Evaluate for malaria.
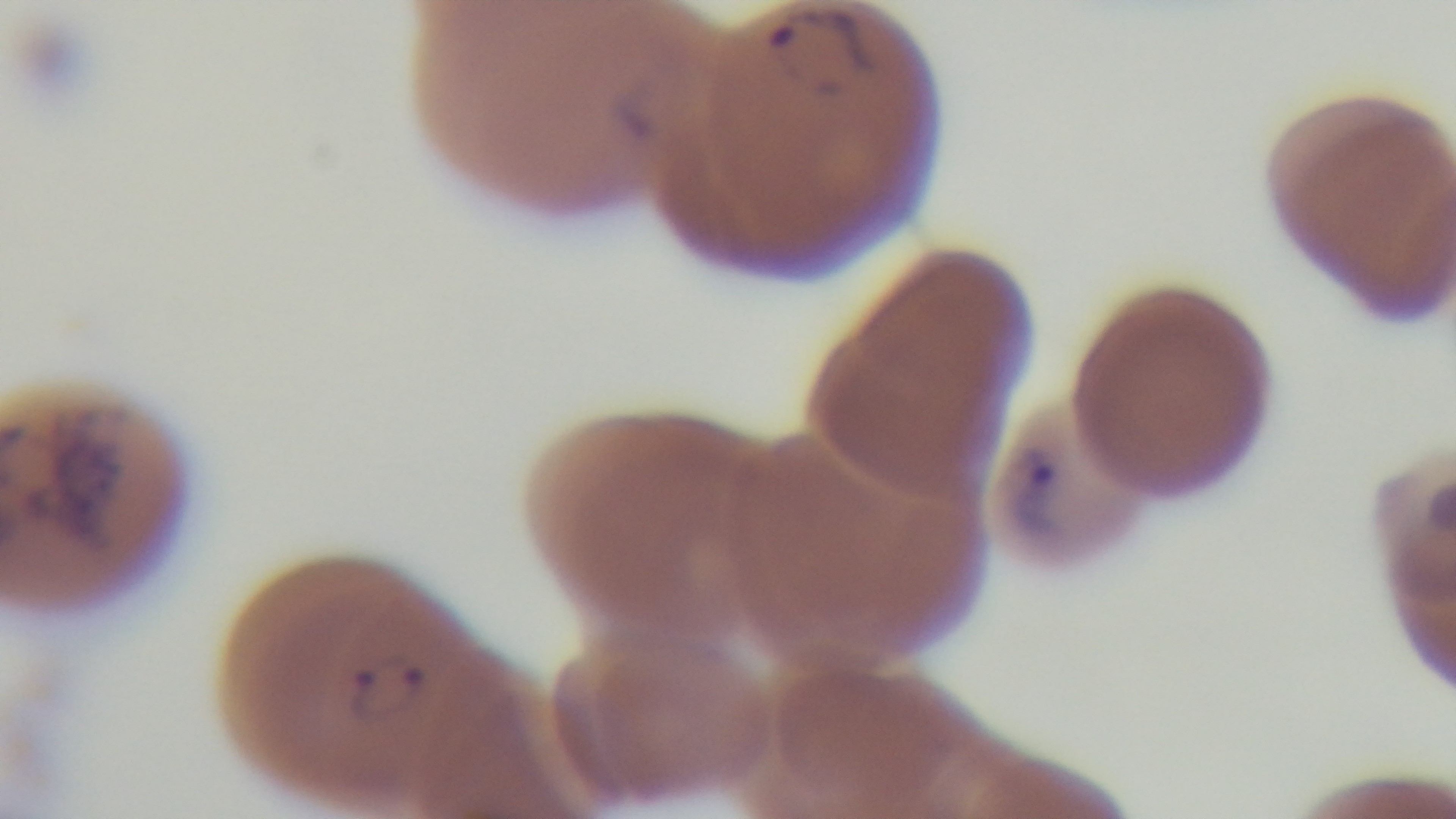
It is infected.

{
  "capture": "mounted 4K digital camera",
  "field_of_view": "one from the slide",
  "preparation": "thin blood film",
  "objective": "100x oil immersion",
  "modality": "light microscopy",
  "stain": "Giemsa"
}